Assess the morphology of the erythrocytes.
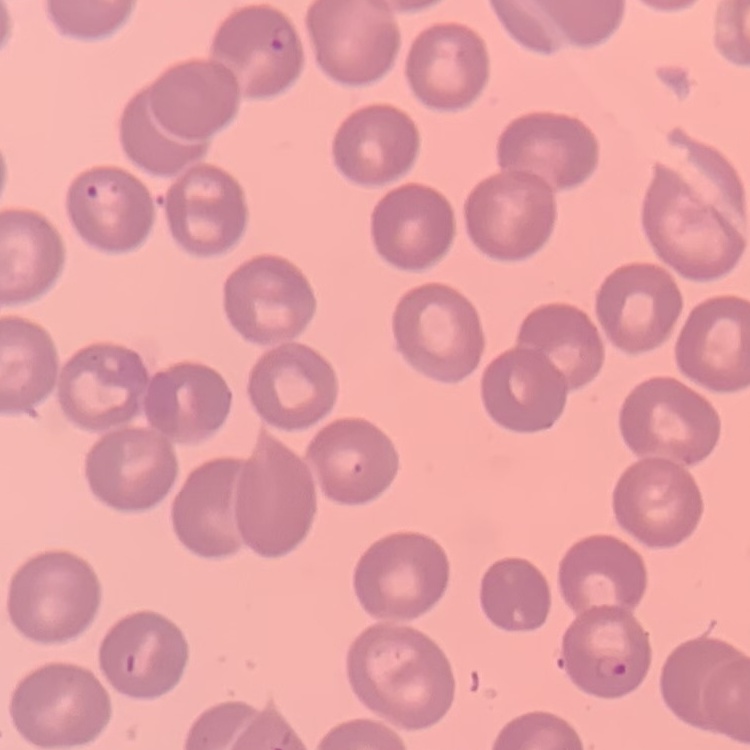
They show no rouleaux formation.

Square crop of a larger photomicrograph. Stained with either Field's or Giemsa. Thin blood film.